Locate every Plasmodium parasite.
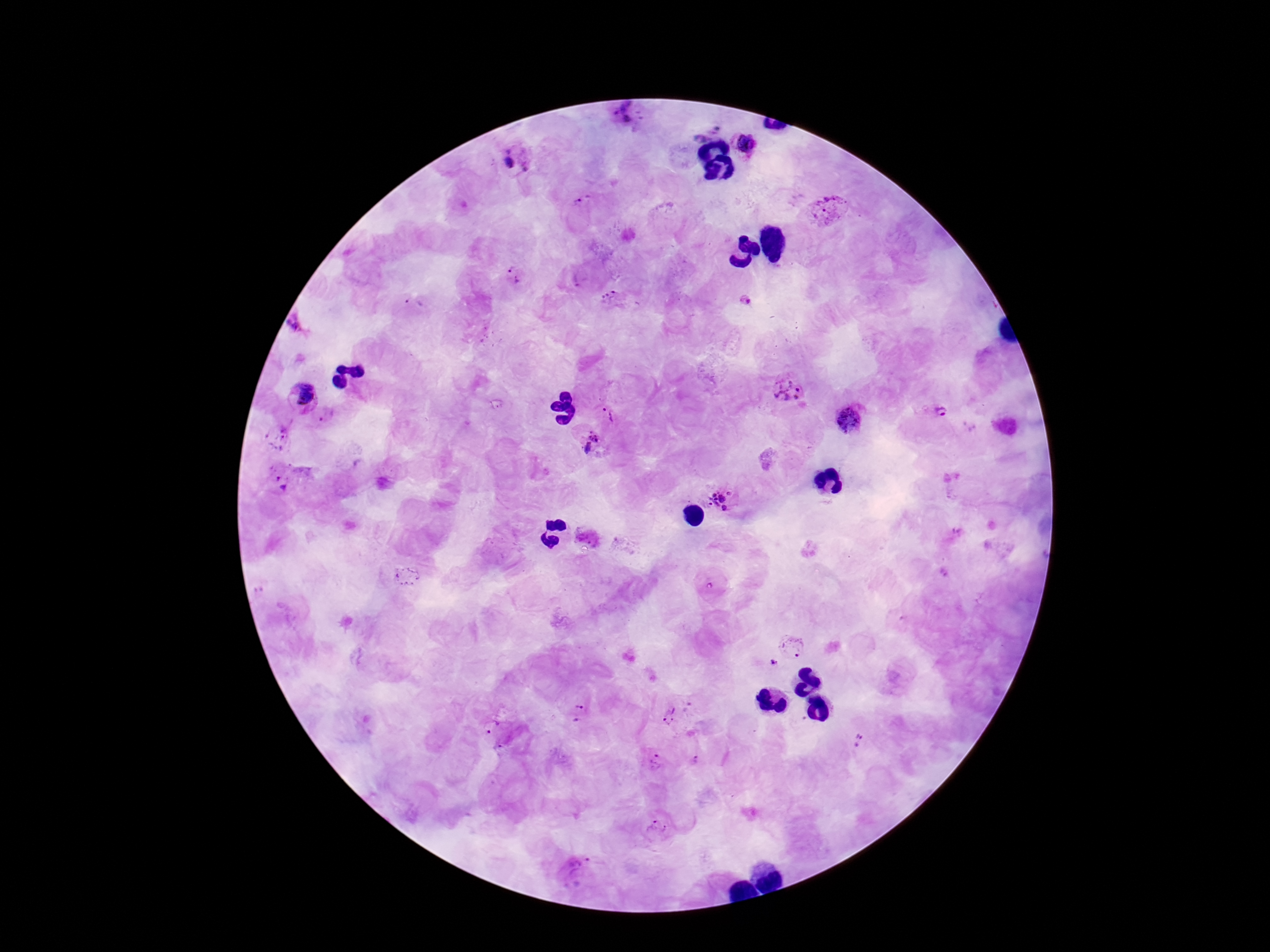
Approximate centers as [x, y] in pixels.
Plasmodium parasites: [621, 112], [704, 128], [748, 145], [518, 155], [832, 209], [579, 212], [514, 273], [615, 300], [746, 300], [414, 302], [299, 326], [788, 387], [301, 397], [940, 410], [611, 412], [851, 418], [279, 438], [589, 442], [283, 476], [722, 499], [407, 575], [794, 644], [774, 664], [578, 714], [671, 716], [489, 726], [859, 739], [696, 760], [655, 764], [657, 826], [580, 870].

Summary:
  - Capture: smartphone camera through the microscope eyepiece
  - Image size: 1270×952 pixels
  - Stain: Giemsa
  - Preparation: thick blood film
  - Magnification: 100x
  - Patient malaria status: positive
  - Field of view: single